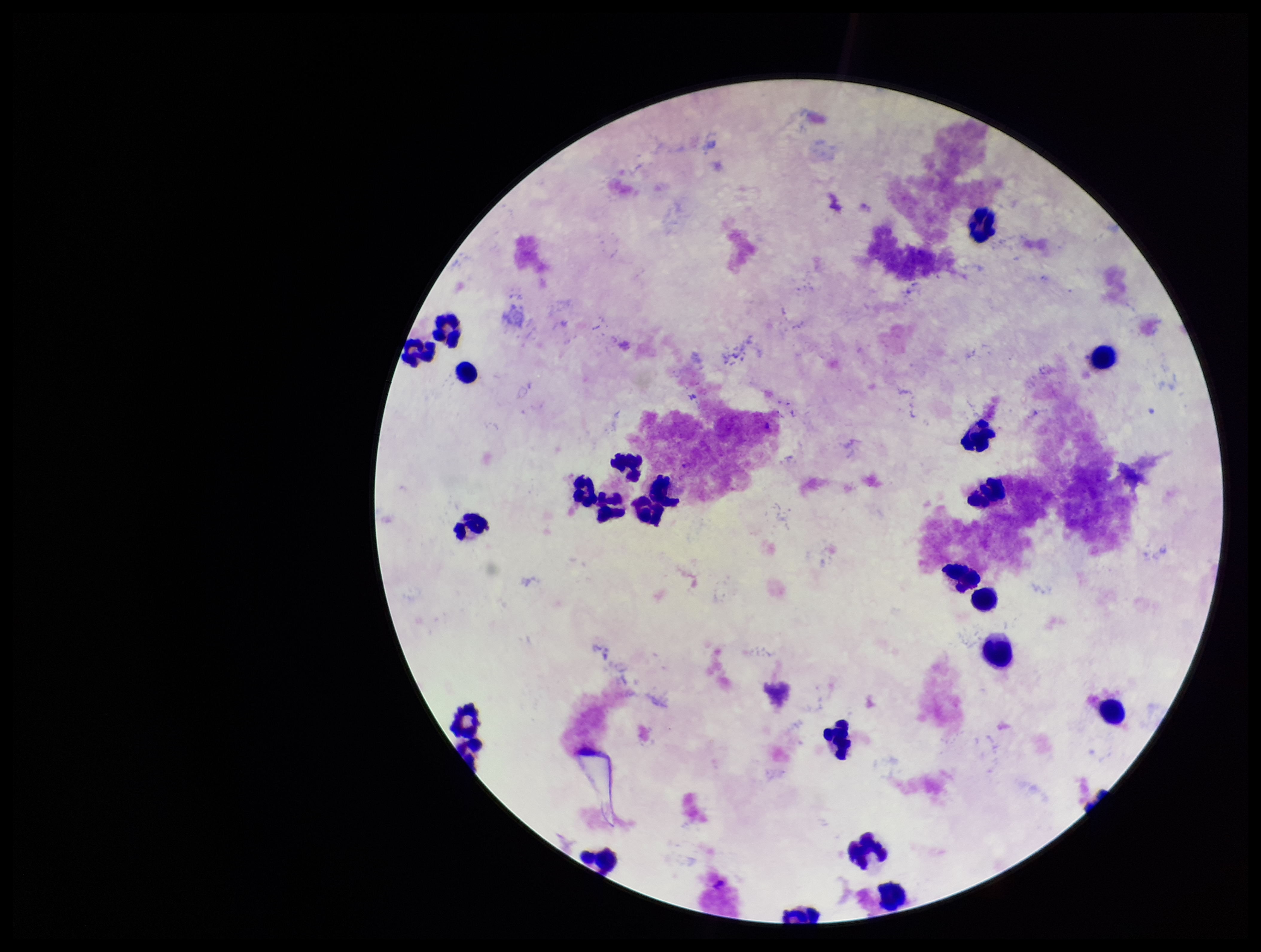 Plasmodium parasites: none identified. One field from this slide. Leukocyte count: 24. Parasite count: 0. Patient malaria status: negative. Smartphone photograph taken through the eyepiece of a microscope. Image is 1261×952 pixels. Stained with Giemsa. Preparation: thick blood smear.